Classify this cell by malaria status.
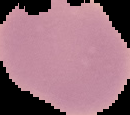
Uninfected.

Summary:
  - Image type: segmented cell region with the area outside set to black
  - Preparation: thin blood smear
  - Image size: 130×115 pixels